Give the extent of all Babesia divergens-infected red blood cells.
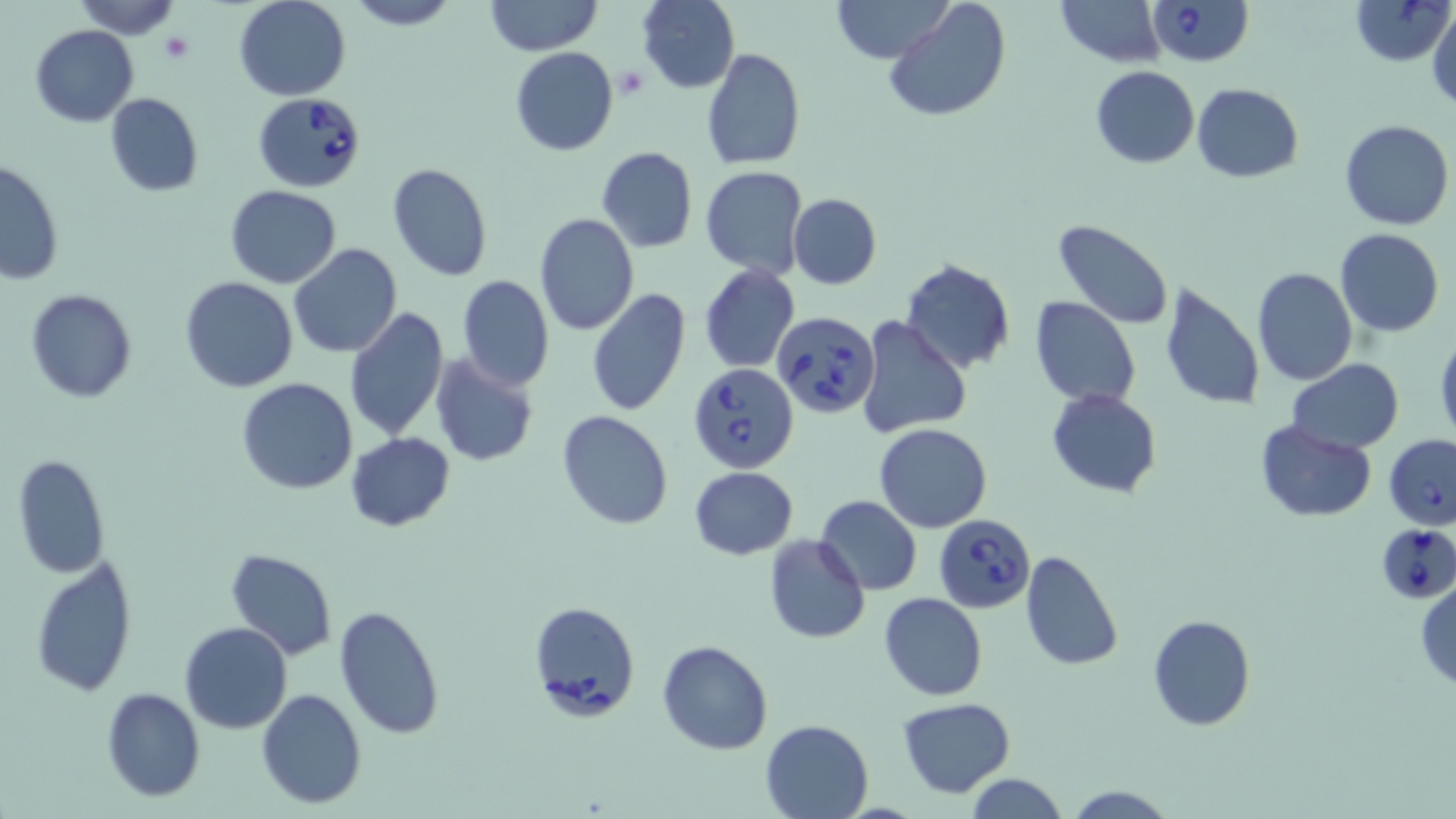

Approximate bounding boxes as (x1, y1, x2, y2) in pixels.
Babesia divergens-infected red blood cells: (1146, 0, 1253, 67), (1351, 0, 1453, 66), (253, 91, 367, 191), (770, 311, 877, 420), (687, 363, 801, 474), (1384, 433, 1456, 528), (934, 513, 1036, 614), (1376, 529, 1453, 608), (529, 601, 640, 720).

Summary:
  - Platelet locations: (160, 30, 194, 64), (615, 65, 650, 101)
  - Uninfected red blood cell locations: (74, 0, 181, 39), (233, 0, 351, 101), (346, 0, 458, 29), (636, 0, 740, 92), (831, 0, 954, 64), (883, 0, 1012, 123), (1054, 0, 1167, 66), (486, 1, 602, 54), (1428, 6, 1456, 110), (30, 25, 139, 126), (510, 47, 619, 156), (701, 47, 806, 171), (1089, 67, 1199, 167), (1191, 84, 1303, 183), (105, 93, 204, 196), (1339, 120, 1455, 231), (596, 146, 698, 253), (0, 160, 65, 283), (387, 162, 494, 282), (700, 166, 807, 278), (225, 185, 341, 287), (788, 193, 881, 289), (535, 213, 639, 335), (1053, 219, 1174, 330), (1335, 228, 1443, 336), (288, 243, 402, 359), (899, 259, 1016, 374), (699, 263, 800, 374), (1251, 266, 1358, 386), (457, 274, 554, 391), (178, 277, 298, 393), (1158, 280, 1265, 413), (24, 288, 138, 402), (586, 289, 691, 417), (1030, 297, 1141, 407), (343, 306, 448, 441), (856, 315, 973, 440), (1434, 329, 1456, 450), (429, 352, 540, 470), (1287, 359, 1404, 453), (236, 377, 359, 494), (1046, 388, 1162, 496), (556, 410, 672, 529), (1255, 420, 1378, 522), (873, 422, 994, 533), (345, 431, 456, 531), (12, 455, 111, 577), (688, 467, 798, 560), (815, 494, 922, 596), (763, 534, 871, 644), (225, 547, 337, 659), (1019, 550, 1125, 672), (30, 555, 135, 698), (1415, 578, 1456, 692), (878, 592, 987, 702), (334, 604, 445, 739), (1148, 614, 1256, 731), (179, 622, 293, 734), (658, 639, 772, 754), (101, 687, 205, 801), (257, 688, 368, 808), (897, 697, 1016, 796), (759, 718, 873, 818), (965, 775, 1069, 817), (1063, 784, 1176, 818)
  - Slide-level diagnosis: Babesia divergens
  - Stain: May-Grünwald-Giemsa
  - Image size: 1456×819 pixels
  - Modality: optical microscopy
  - Preparation: thin blood smear
  - Magnification: 1000x
  - Field of view: single